Name the parasite shown.
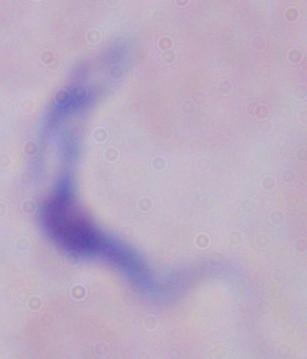

This is a trypanosome.

modality = photomicrograph
magnification = 1000x